Identify the cell.
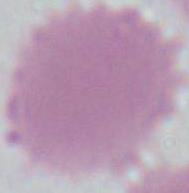
An erythrocyte.

Photomicrograph. Captured at 1000x magnification.